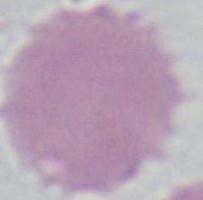 An erythrocyte is seen. Micrograph. Captured at 1000x magnification.